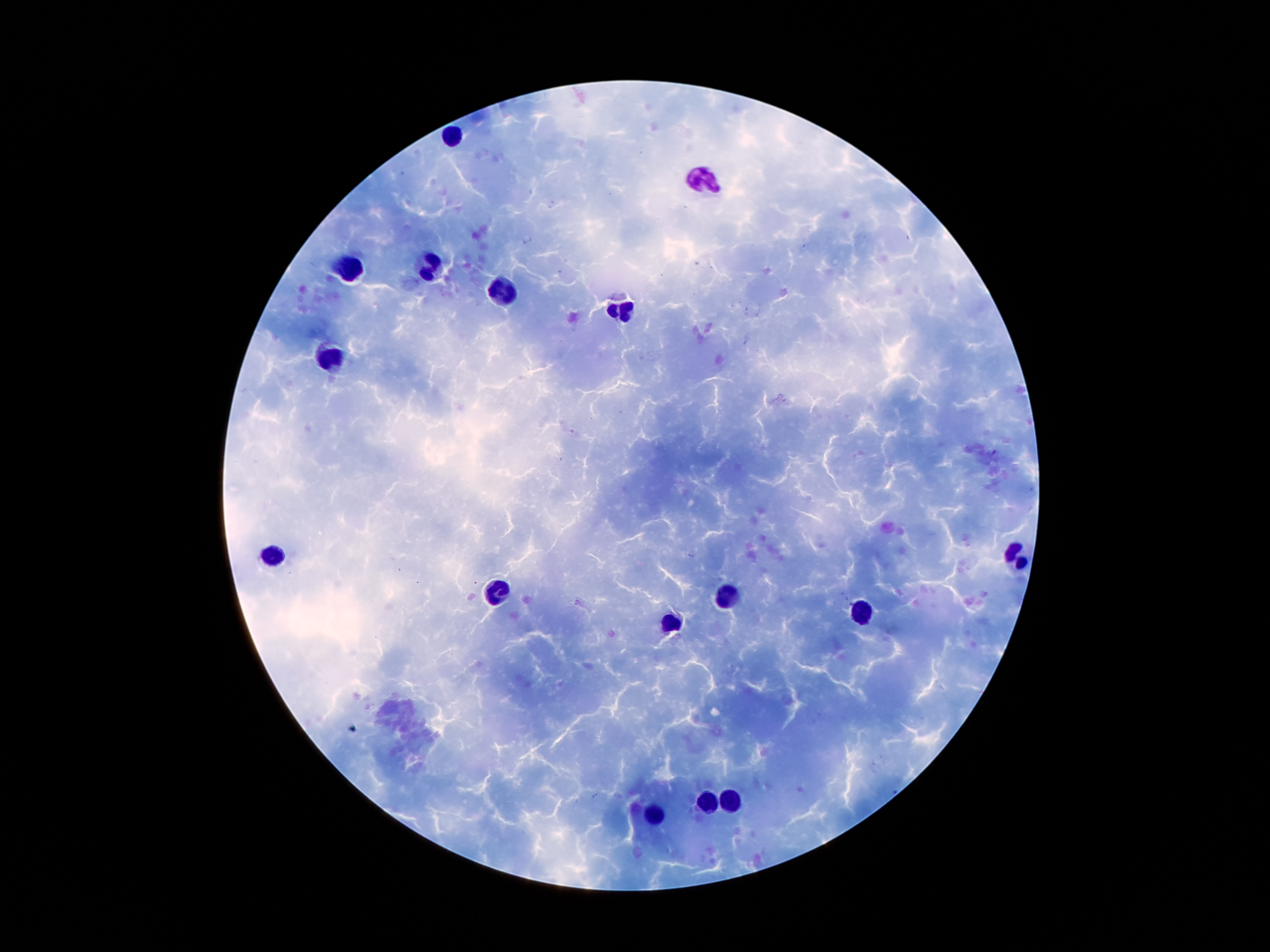
Approximate centers as {x, y} in pixels. Leukocyte locations: {455, 133}, {703, 184}, {349, 270}, {429, 270}, {502, 292}, {623, 310}, {334, 356}, {1019, 551}, {272, 555}, {500, 593}, {725, 595}, {864, 615}, {670, 622}, {710, 800}, {732, 800}, {654, 818}. Plasmodium parasites: not detected. Single field of view. Giemsa stain. 100x magnification. Thick peripheral-blood smear. Image is 1270×952 pixels. Patient malaria status: positive for Plasmodium falciparum. Smartphone photograph taken through the microscope eyepiece.